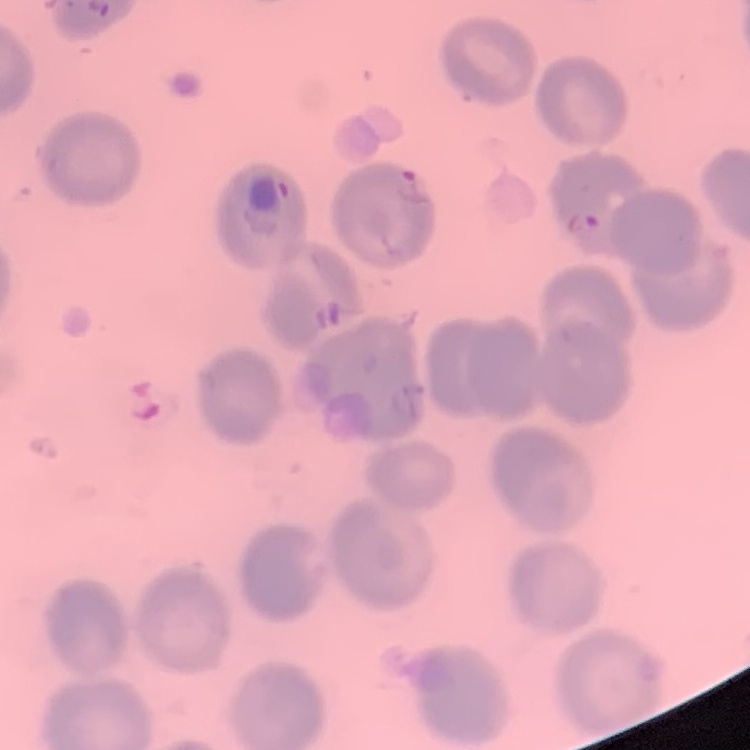

Summary:
  - Red blood cell morphology: no rouleaux formation
  - Stain: Field's or Giemsa
  - Preparation: thin peripheral smear
  - Image type: one tile cut from a larger photomicrograph